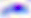

Summary:
  - Modality: micrograph
  - Magnification: 400x
  - Identification: Toxoplasma gondii